Point out every malaria parasite.
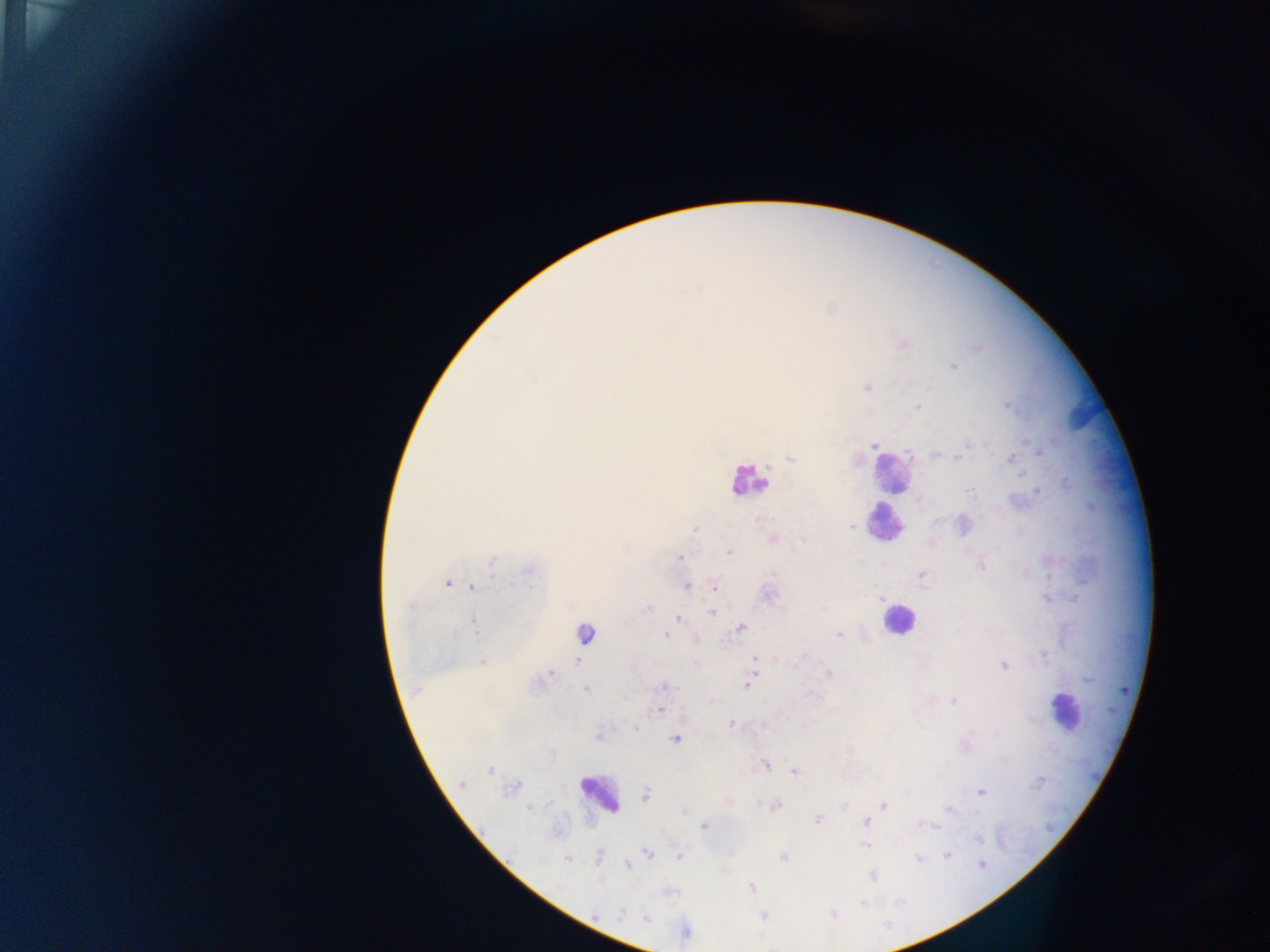

Approximate centers as [x, y] in pixels.
Malaria parasites: [691, 288], [698, 289], [977, 347], [954, 367], [533, 377], [868, 388], [1007, 405], [917, 407], [1054, 440], [1029, 441], [875, 445], [909, 452], [1039, 454], [937, 455], [958, 456], [1011, 457], [791, 458], [768, 465], [1018, 474], [1036, 491], [971, 494], [853, 527], [695, 528], [773, 538], [803, 541], [729, 552], [678, 558], [491, 563], [982, 565], [527, 570], [922, 575], [448, 583], [473, 587], [687, 587], [714, 590], [884, 601], [648, 607], [711, 614], [678, 618], [473, 621], [741, 627], [584, 634], [839, 634], [665, 636], [695, 640], [754, 654], [803, 655], [1044, 656], [481, 661], [576, 662], [1005, 665], [758, 672], [551, 673], [830, 673], [660, 687], [745, 687], [585, 690], [954, 702], [661, 710], [731, 724], [635, 727], [676, 740], [766, 766], [489, 770], [795, 772], [462, 783], [981, 791], [647, 795], [883, 804], [777, 806], [528, 807], [950, 810], [684, 811], [817, 819], [865, 821], [919, 825], [703, 827], [939, 827], [977, 840], [865, 846], [649, 853], [948, 855], [679, 856], [784, 856], [600, 858], [919, 859], [567, 860], [979, 864], [626, 865], [874, 876], [752, 888], [900, 901], [862, 902], [622, 910], [833, 914], [764, 916], [647, 919].

Leukocyte locations: [754, 475], [894, 483], [889, 528], [898, 621], [1063, 713], [599, 798]. Collected in Ghana. Thick blood film. Image is 1270×952 pixels. Mobile-phone photograph taken through the microscope. One field of view.